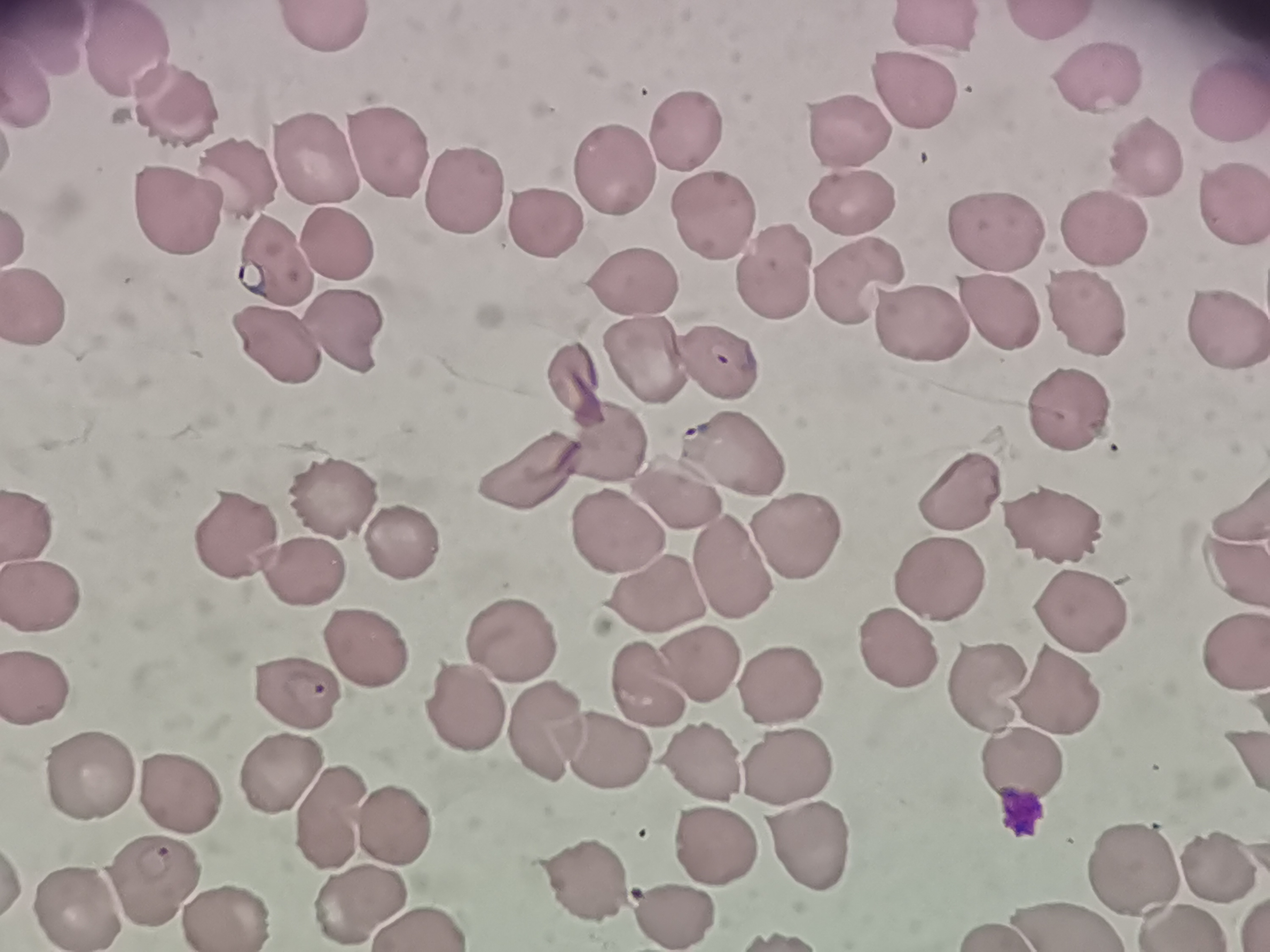
cell locations = approximate object centers, in pixels from the top-left corner: (x=1052, y=26), (x=321, y=27), (x=935, y=28), (x=49, y=43), (x=143, y=53), (x=1104, y=75), (x=910, y=78), (x=34, y=84), (x=1225, y=94), (x=171, y=100), (x=856, y=129), (x=688, y=132), (x=386, y=148), (x=1153, y=159), (x=313, y=162), (x=609, y=169), (x=232, y=177), (x=457, y=190), (x=1234, y=198), (x=178, y=208), (x=852, y=209), (x=714, y=214), (x=539, y=221), (x=1101, y=225), (x=1003, y=229), (x=21, y=230), (x=341, y=246), (x=854, y=273), (x=776, y=275), (x=631, y=284), (x=45, y=304), (x=1001, y=311), (x=1089, y=312), (x=906, y=315), (x=1225, y=321), (x=350, y=339), (x=286, y=346), (x=637, y=356), (x=709, y=358), (x=582, y=382), (x=1074, y=396), (x=614, y=447), (x=737, y=462), (x=532, y=466), (x=673, y=478), (x=968, y=486), (x=337, y=494), (x=1242, y=500), (x=36, y=521), (x=1048, y=525), (x=796, y=530), (x=619, y=533), (x=229, y=535), (x=407, y=540), (x=1230, y=559), (x=729, y=560), (x=309, y=568), (x=942, y=574), (x=43, y=592), (x=1082, y=618), (x=902, y=641), (x=522, y=644), (x=1236, y=644), (x=368, y=651), (x=695, y=653), (x=778, y=678), (x=981, y=678), (x=645, y=679), (x=43, y=683), (x=1057, y=688), (x=297, y=692), (x=463, y=695), (x=552, y=734), (x=606, y=750), (x=700, y=762), (x=1021, y=762), (x=783, y=767), (x=272, y=771), (x=87, y=772), (x=165, y=788), (x=332, y=810), (x=390, y=823), (x=810, y=845), (x=713, y=847), (x=1130, y=856), (x=1210, y=866), (x=584, y=878), (x=165, y=881), (x=78, y=901), (x=676, y=902), (x=360, y=907), (x=1178, y=916), (x=225, y=917), (x=430, y=919), (x=1070, y=922), (x=985, y=925)
preparation = thin blood smear
capture = smartphone through the microscope eyepiece
image size = 1270×952 pixels
field of view = single
stain = Giemsa